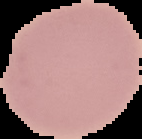
Summary:
  - Preparation: thin blood smear
  - Image type: segmented cell region with the area outside set to black
  - Malaria status: uninfected
  - Image size: 142×139 pixels